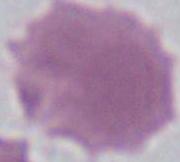
Captured at 1000x magnification. A red blood cell is seen. Micrograph.